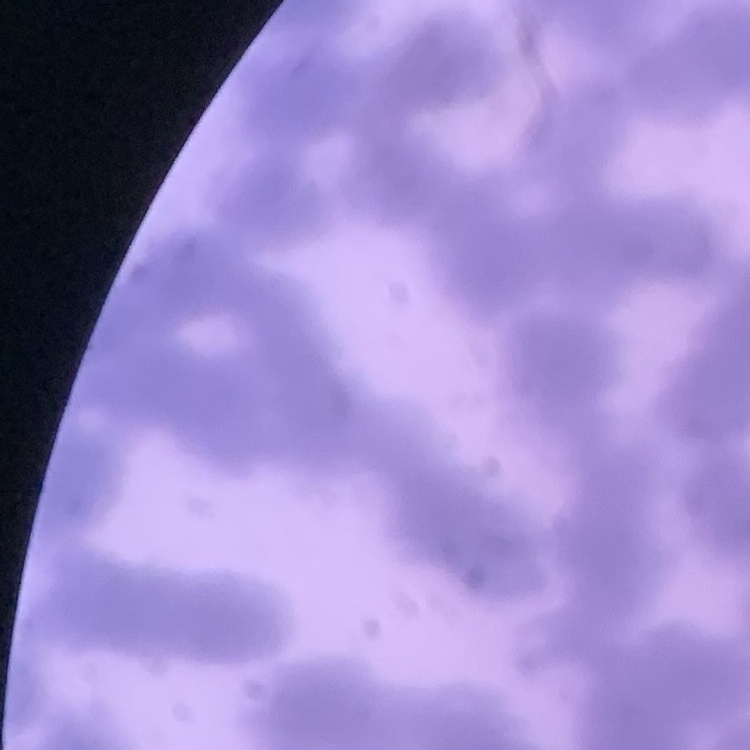
Summary:
  - Red blood cell morphology: rouleaux formation
  - Image type: one tile cut from a larger photomicrograph
  - Stain: Field's or Giemsa
  - Preparation: thin blood film